Name the cell type shown.
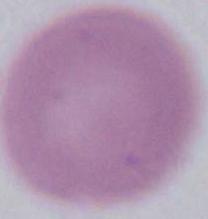

This is an erythrocyte.

modality = photomicrograph
magnification = 1000x